Classify this cell by malaria status.
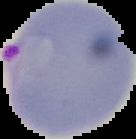
It is parasitized.

Summary:
  - Image type: cell region segmented out of the field of view; surrounding area masked to black
  - Preparation: thin blood smear
  - Image size: 136×139 pixels